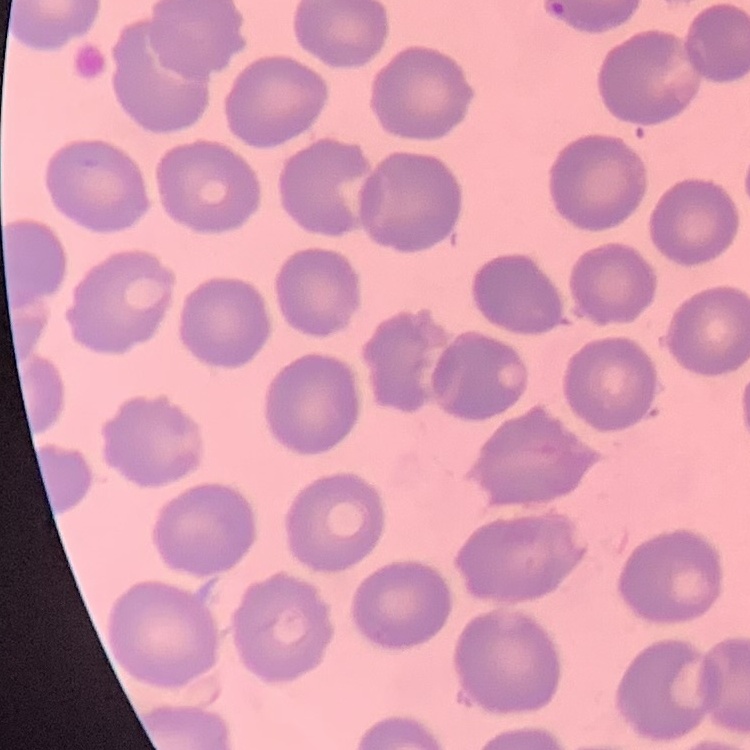 The red blood cells show no rouleaux formation. Stained with either Field's or Giemsa. Thin blood film. One tile cut from a larger photomicrograph.